Identify the blood parasite species.
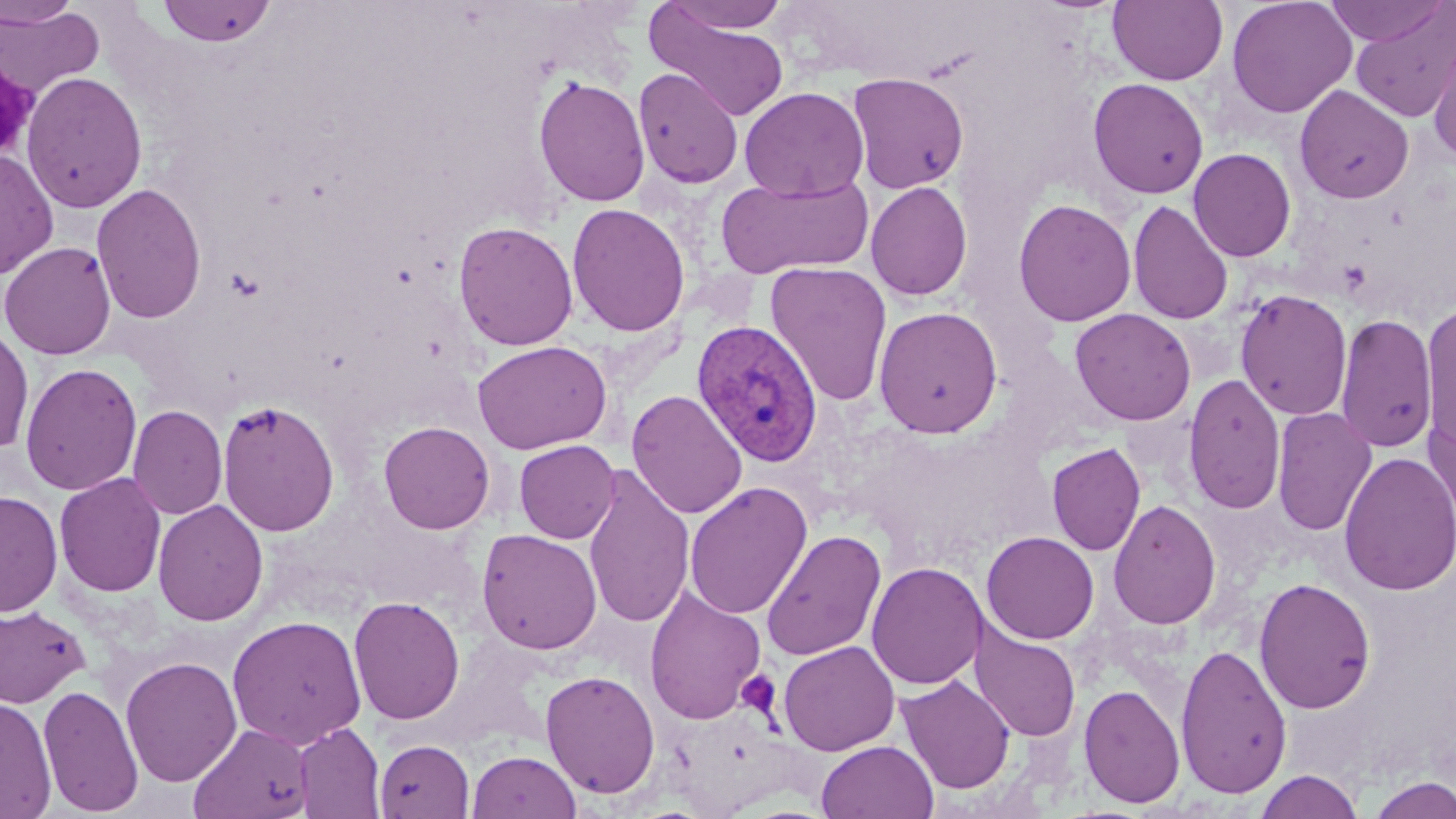

Plasmodium vivax.

stain = May-Grünwald-Giemsa
preparation = thin blood smear
magnification = 1000x
platelet locations = approximate bounding boxes as (x1,y1)-(x2,y2) corner pairs in pixels: (737,670)-(780,718)
uninfected red blood cell locations = approximate bounding boxes as (x1,y1)-(x2,y2) corner pairs in pixels: (156,0)-(277,47), (1108,0)-(1228,86), (1226,0)-(1357,118), (1323,0)-(1450,47), (0,1)-(82,28), (662,1)-(792,34), (0,3)-(105,102), (1349,5)-(1456,125), (645,7)-(792,120), (1427,28)-(1456,163), (633,68)-(744,189), (21,70)-(148,214), (847,72)-(970,194), (532,75)-(651,207), (1088,78)-(1209,199), (1294,85)-(1415,203), (739,86)-(869,201), (1188,148)-(1296,262), (0,149)-(59,280), (716,173)-(874,280), (865,181)-(973,302), (91,182)-(208,325), (1013,198)-(1137,327), (1128,199)-(1233,325), (567,203)-(690,337), (453,221)-(579,351), (1,241)-(116,359), (765,262)-(892,407), (1235,289)-(1352,420), (1420,302)-(1456,454), (873,306)-(1003,438), (1070,308)-(1196,426), (1335,312)-(1438,454), (0,325)-(34,455), (472,341)-(612,454), (20,362)-(142,496), (1183,373)-(1286,514), (626,389)-(747,520), (217,399)-(340,536), (1424,403)-(1456,533), (128,405)-(227,520), (1271,406)-(1377,537), (378,421)-(495,534), (514,439)-(620,544), (1046,443)-(1146,556), (1339,451)-(1456,596), (582,465)-(695,629), (54,472)-(167,597), (684,481)-(813,619), (0,490)-(63,618), (153,499)-(269,626), (1108,499)-(1221,630), (477,529)-(602,655), (761,529)-(886,661), (981,530)-(1100,644), (866,561)-(987,690), (1253,576)-(1376,714), (644,587)-(766,725), (348,596)-(465,725), (0,604)-(90,708), (226,614)-(367,749), (969,625)-(1081,742), (778,640)-(900,755), (1175,643)-(1292,799), (120,656)-(241,786), (540,669)-(660,799), (897,675)-(1015,794), (38,683)-(144,817), (1079,684)-(1186,808), (0,695)-(56,818), (189,722)-(314,819), (293,722)-(385,818), (375,739)-(475,818), (816,740)-(939,819), (466,750)-(581,819), (1254,770)-(1364,818), (1365,775)-(1456,819)
image size = 1456×819 pixels
Plasmodium vivax-infected red blood cell locations = approximate bounding boxes as (x1,y1)-(x2,y2) corner pairs in pixels: (691,319)-(823,467)
modality = light microscopy
field of view = single